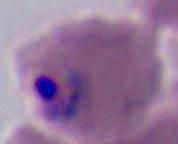

Summary:
  - Magnification: 400x or 1000x
  - Identification: Plasmodium
  - Modality: photomicrograph